Report the malaria status of this cell.
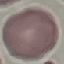
It is uninfected.

image type = cell patch, automatically extracted from a larger field of view and resized to 64 × 64 pixels
stain = Giemsa
preparation = thin blood film
capture = smartphone through the microscope eyepiece